Assess the morphology of the erythrocytes.
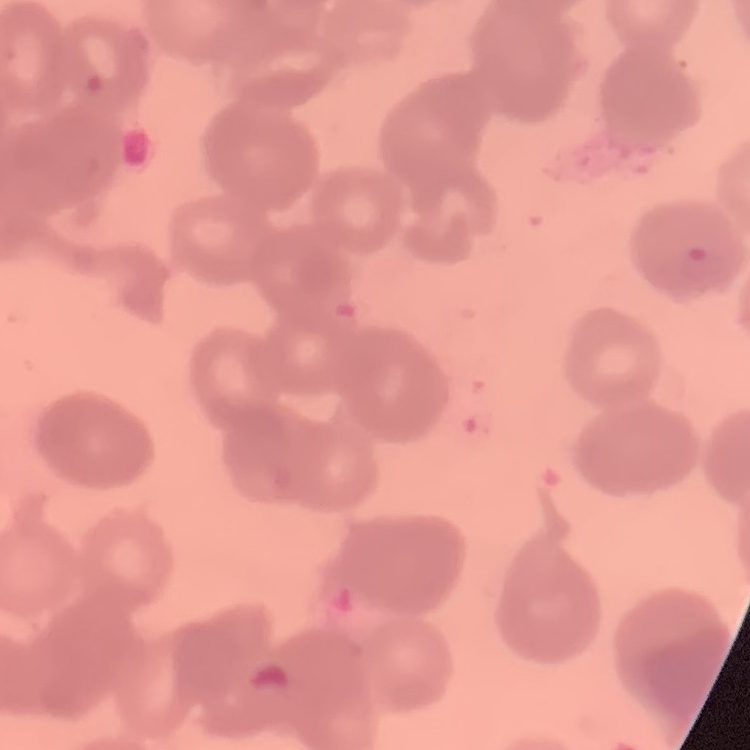
Rouleaux formation.

image type = one tile cut from a larger photomicrograph
preparation = thin blood smear
stain = Field's or Giemsa